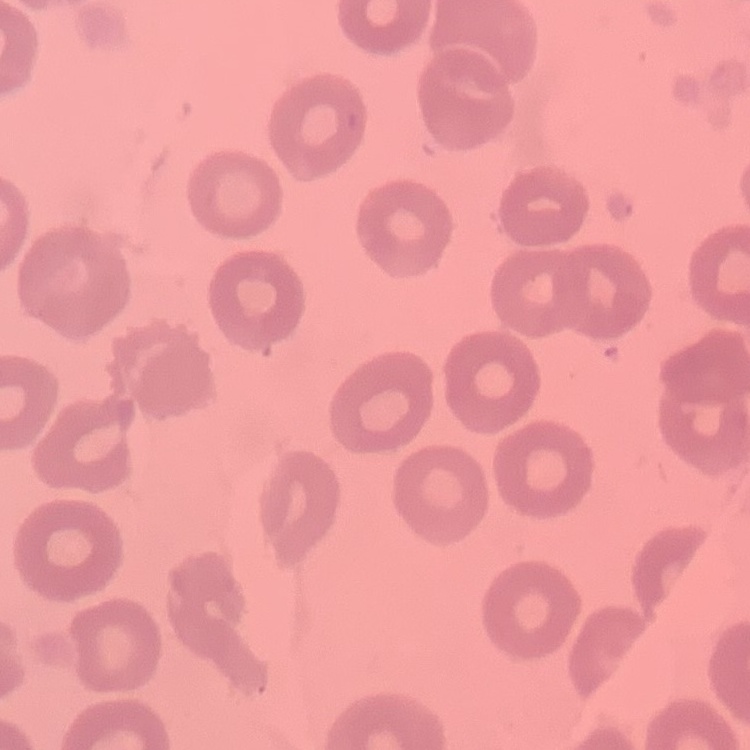 The erythrocytes exhibit no rouleaux formation. Field's or Giemsa stain. Thin blood smear. Square crop of a larger photomicrograph.